Report the malaria status of this cell.
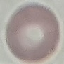

It is uninfected.

Giemsa-stained preparation. Acquired by smartphone through the microscope eyepiece. Automatically extracted cell patch, resized to 64 × 64 pixels. Thin blood film.